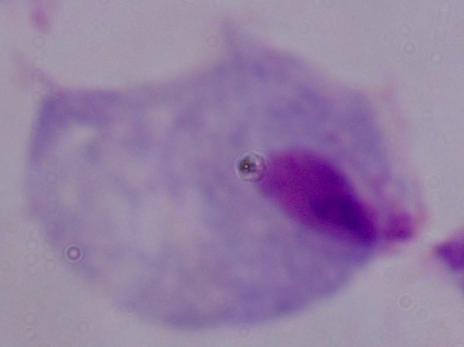

magnification = 1000x
identification = trichomonad
modality = micrograph